Classify this cell by malaria status.
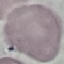
Uninfected.

Giemsa-stained preparation. Thin smear of blood. Automatically extracted cell patch, resized to 64 × 64 pixels. Acquired by smartphone through the microscope eyepiece.